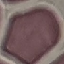
result = no malaria parasites seen
capture = smartphone through the microscope eyepiece
preparation = thin blood film
image type = automatically extracted cell patch, resized to 64 × 64 pixels
stain = Giemsa